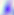

modality = photomicrograph
magnification = 400x
identification = Toxoplasma gondii